Point out each Plasmodium parasite.
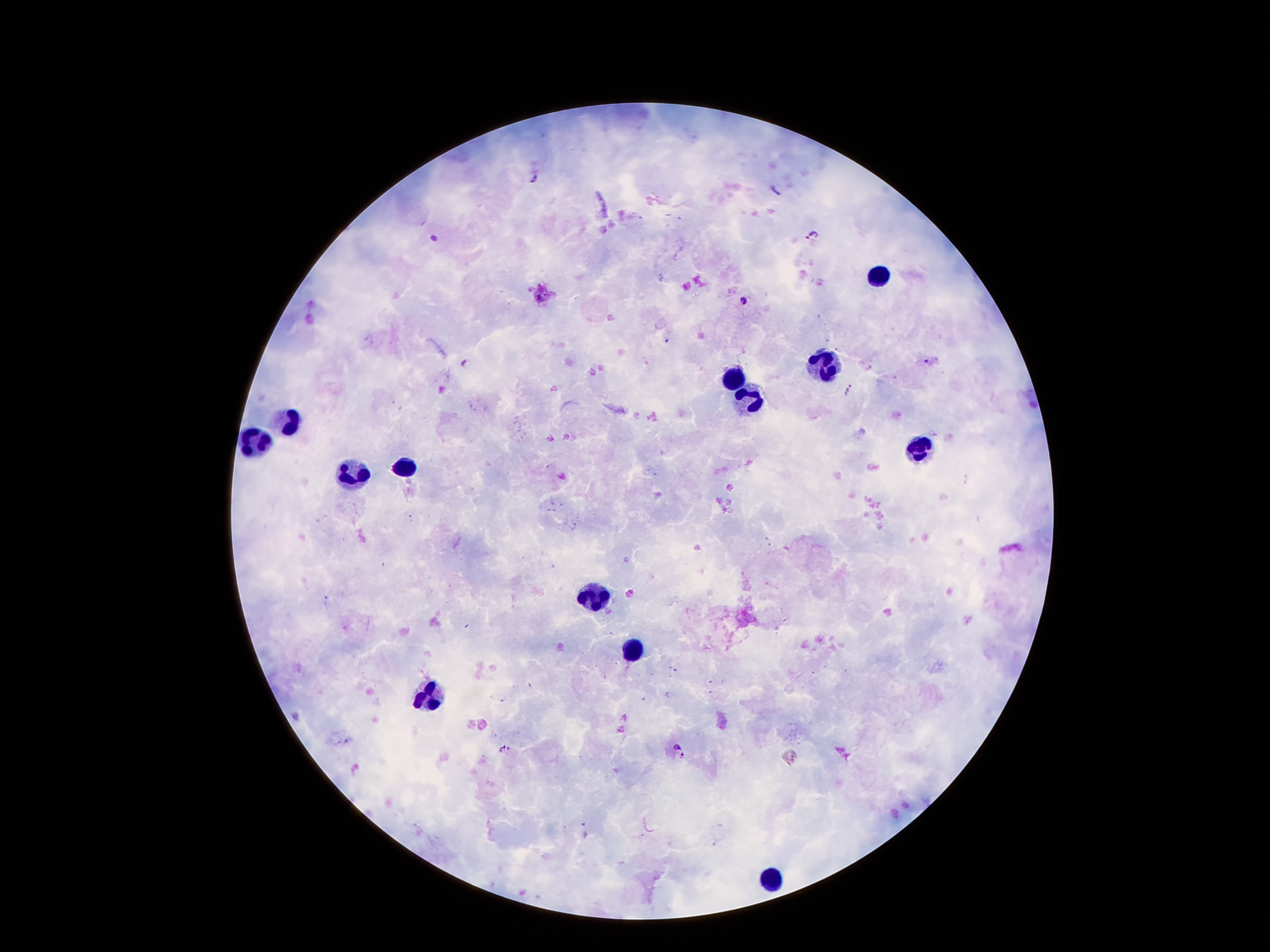
Approximate centers as [x, y] in pixels.
Plasmodium parasites: [533, 180], [777, 189], [811, 236], [434, 238], [743, 300], [928, 361], [465, 362], [849, 389], [506, 748], [680, 750].

Summary:
  - Leukocyte locations: [880, 276], [822, 365], [734, 376], [747, 392], [289, 420], [256, 436], [919, 449], [408, 465], [353, 471], [592, 595], [631, 647], [428, 695], [773, 875]
  - Preparation: thick blood smear
  - Image size: 1270×952 pixels
  - Field of view: one from this slide
  - Magnification: 100x
  - Capture: smartphone through the microscope eyepiece
  - Patient malaria status: infected with Plasmodium falciparum
  - Stain: Giemsa